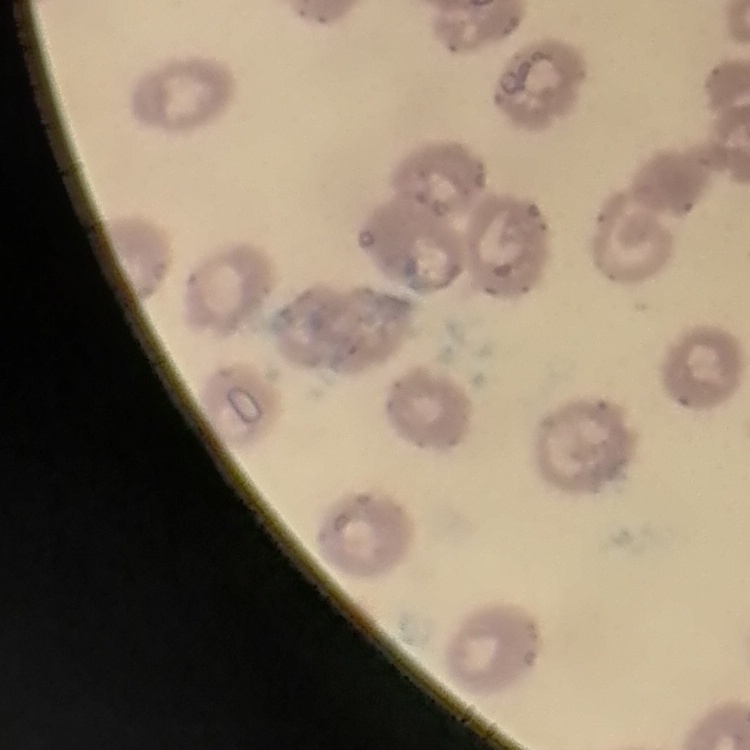

Summary:
  - Red blood cell morphology: no rouleaux formation
  - Image type: square crop of a larger photomicrograph
  - Preparation: thin blood film
  - Stain: Field's or Giemsa